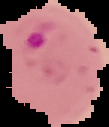
Summary:
  - Result: malaria parasites identified
  - Image size: 109×127 pixels
  - Preparation: thin blood smear
  - Image type: cell region segmented out of the field of view; surrounding area masked to black